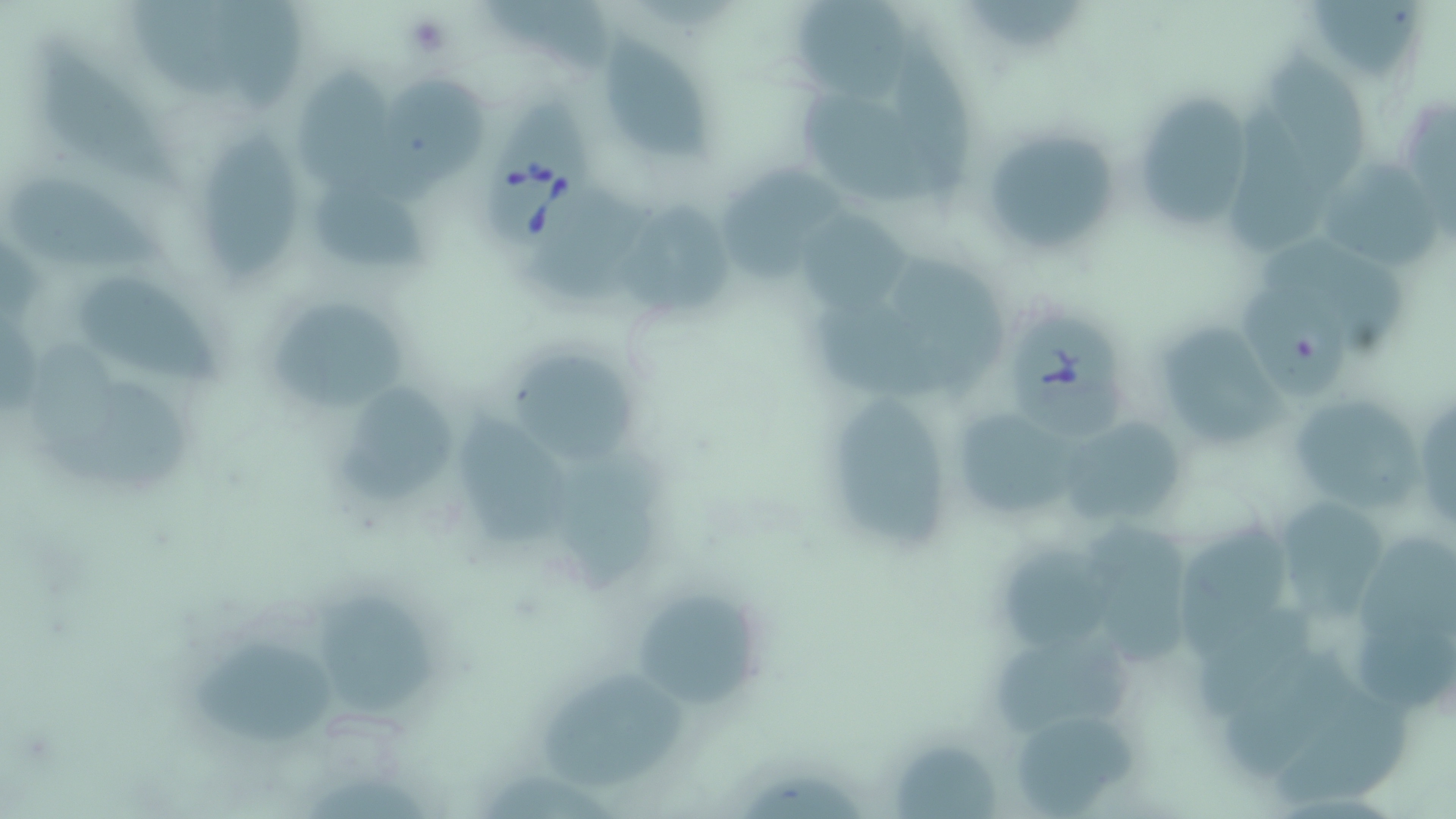

slide-level diagnosis = Babesia divergens
preparation = thin blood smear
Babesia divergens-infected red blood cell locations = approximate bounding boxes as (x1, y1, x2, y2) in pixels: (490, 89, 599, 252), (1008, 306, 1125, 436)
magnification = 1000x
modality = light microscopy
uninfected red blood cell locations = approximate bounding boxes as (x1, y1, x2, y2) in pixels: (1299, 0, 1429, 88), (140, 2, 258, 108), (216, 2, 307, 110), (487, 2, 615, 69), (797, 3, 913, 103), (971, 3, 1088, 53), (888, 19, 973, 209), (41, 38, 178, 188), (609, 38, 714, 162), (1262, 56, 1368, 199), (296, 67, 396, 193), (374, 78, 486, 209), (1131, 89, 1257, 239), (800, 90, 936, 206), (1222, 107, 1324, 251), (978, 124, 1123, 263), (202, 133, 301, 282), (719, 158, 843, 282), (1321, 159, 1444, 278), (15, 179, 171, 273), (314, 180, 440, 277), (522, 187, 653, 307), (619, 204, 734, 319), (794, 211, 911, 317), (1261, 241, 1415, 353), (886, 255, 1003, 403), (79, 274, 227, 391), (263, 292, 412, 413), (1236, 292, 1350, 405), (811, 302, 944, 400), (1160, 329, 1297, 444), (507, 354, 638, 465), (42, 382, 203, 495), (830, 389, 952, 551), (1286, 389, 1429, 520), (335, 390, 459, 507), (1411, 392, 1456, 531), (945, 401, 1082, 526), (463, 413, 580, 551), (1056, 425, 1186, 526), (554, 458, 668, 596), (1276, 495, 1386, 619), (1172, 513, 1290, 664), (1087, 526, 1193, 673), (1354, 536, 1456, 645), (1006, 548, 1118, 657), (632, 588, 763, 710), (318, 593, 441, 714), (1195, 606, 1312, 723), (1354, 612, 1456, 710), (188, 637, 341, 741), (988, 640, 1135, 735), (1220, 653, 1357, 783), (535, 674, 686, 793), (1270, 692, 1413, 810), (1013, 717, 1144, 819), (892, 741, 1006, 819)
image size = 1456×819 pixels
stain = May-Grünwald-Giemsa
field of view = single